Point out every malaria parasite and every leukocyte.
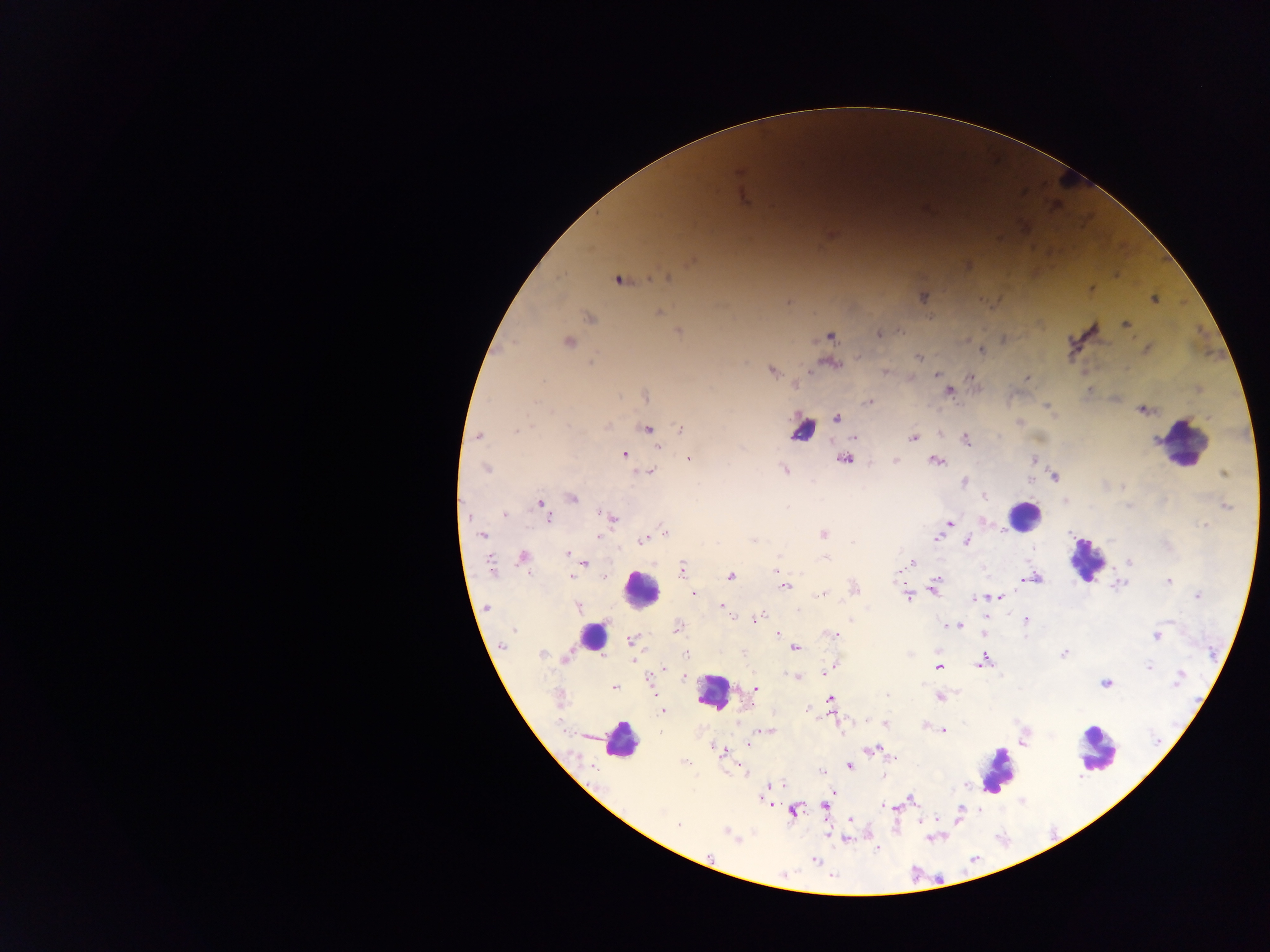
Approximate centers as x y in pixels.
Malaria parasites: 743 198; 666 277; 617 280; 923 297; 1154 299; 788 302; 660 311; 589 318; 1125 324; 679 332; 901 332; 879 333; 830 336; 1003 340; 568 341; 1146 348; 981 350; 918 358; 591 362; 834 365; 772 371; 885 371; 936 374; 969 377; 1027 378; 1089 390; 949 392; 645 396; 869 402; 1047 407; 1143 410; 837 418; 1019 423; 606 426; 648 428; 681 429; 516 430; 479 436; 855 437; 913 437; 966 440; 658 446; 624 454; 690 459; 845 460; 895 460; 1034 460; 936 461; 485 469; 784 470; 650 472; 1223 474; 1054 477; 964 482; 1122 487; 983 496; 573 498; 1066 502; 540 504; 1227 506; 1128 507; 504 514; 548 518; 612 518; 949 523; 1203 524; 664 530; 823 534; 482 535; 599 537; 936 539; 643 540; 753 540; 968 541; 853 542; 567 554; 523 557; 826 558; 1130 562; 585 563; 910 564; 491 567; 682 569; 900 569; 731 576; 572 577; 605 578; 1034 578; 1169 581; 1120 585; 785 586; 934 588; 855 589; 693 593; 821 595; 907 596; 1198 596; 996 597; 974 599; 721 606; 488 607; 577 607; 797 609; 755 619; 1026 619; 851 620; 948 626; 956 626; 678 627; 515 630; 778 634; 832 635; 1156 636; 631 641; 795 647; 686 653; 542 654; 1064 654; 567 657; 632 660; 983 662; 938 667; 1149 667; 831 668; 664 670; 796 677; 684 678; 1179 678; 1106 683; 615 688; 755 688; 886 695; 558 698; 941 698; 830 699; 807 710; 663 711; 885 724; 925 726; 768 730; 943 730; 748 744; 872 749; 723 751; 893 758; 684 762; 850 766; 821 771; 779 785; 910 799; 825 805; 886 807; 794 811; 850 820; 677 825; 727 833; 846 839; 815 860.
Leukocytes: 1074 178; 802 431; 1184 444; 1024 516; 1086 559; 641 588; 592 635; 713 692; 620 741; 1096 750; 992 764.

Summary:
  - Image size: 1270×952 pixels
  - Field of view: single
  - Capture: mobile-phone photograph through a microscope
  - Country: Ghana
  - Preparation: thick blood film